Report the malaria status of this cell.
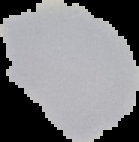
It is uninfected.

Segmented cell region on a black background. From a thin blood smear. Image is 139×142 pixels.